Locate every malaria parasite.
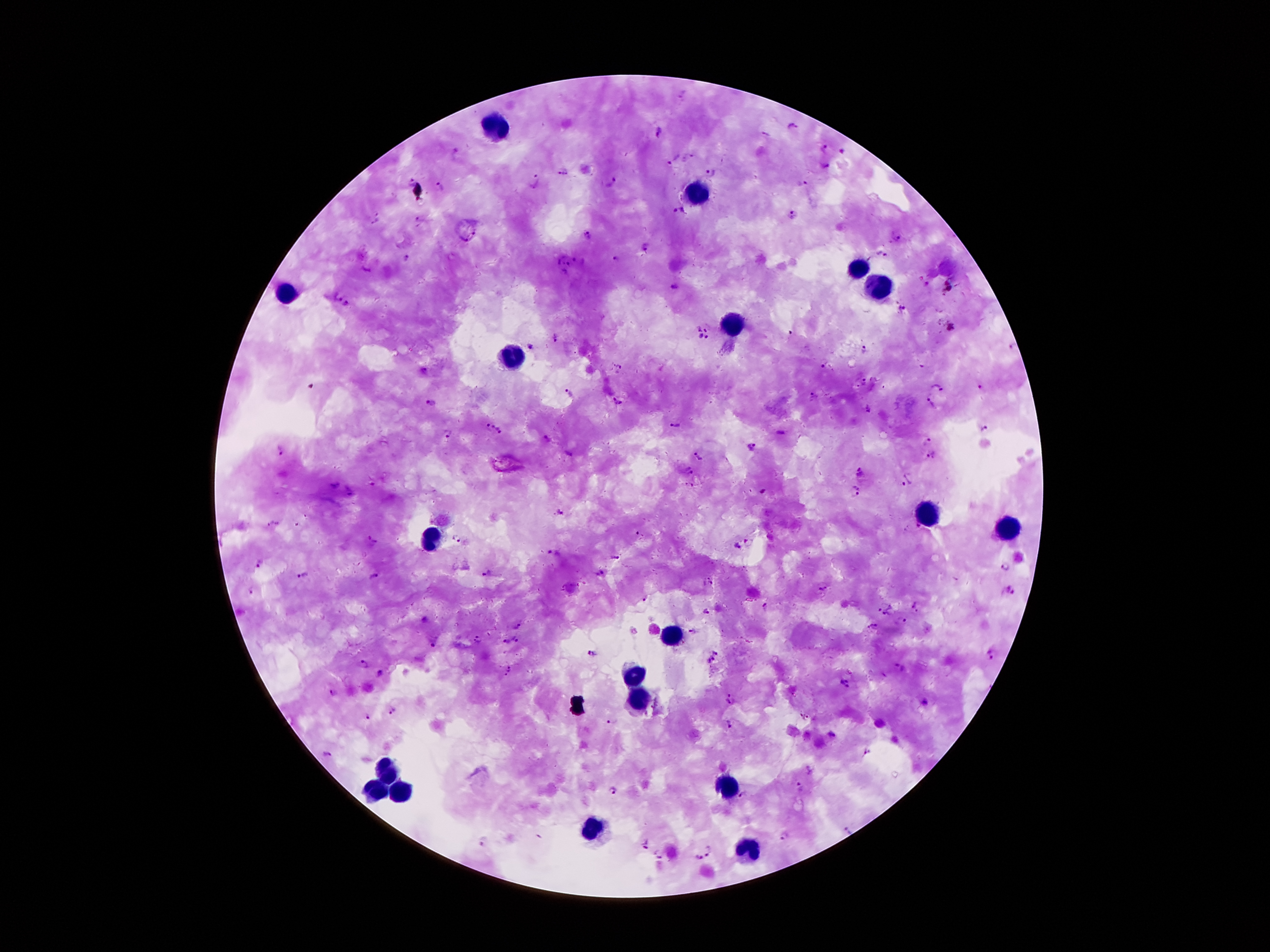

Approximate centers as {x, y} in pixels.
Malaria parasites: {683, 95}, {792, 126}, {660, 132}, {765, 135}, {825, 147}, {842, 151}, {674, 160}, {825, 168}, {563, 173}, {711, 173}, {538, 176}, {613, 181}, {412, 182}, {801, 183}, {441, 188}, {677, 211}, {794, 214}, {375, 217}, {420, 219}, {588, 236}, {897, 239}, {646, 247}, {881, 254}, {618, 258}, {407, 259}, {578, 259}, {567, 264}, {675, 287}, {345, 303}, {900, 309}, {701, 334}, {554, 337}, {529, 347}, {1010, 347}, {863, 349}, {824, 364}, {620, 368}, {424, 373}, {865, 382}, {936, 386}, {980, 388}, {568, 395}, {814, 396}, {930, 396}, {430, 402}, {618, 403}, {867, 409}, {488, 426}, {674, 426}, {984, 429}, {449, 433}, {503, 433}, {780, 433}, {547, 438}, {927, 441}, {753, 447}, {281, 450}, {569, 454}, {697, 456}, {932, 456}, {689, 471}, {859, 474}, {907, 479}, {690, 486}, {763, 491}, {856, 492}, {558, 512}, {274, 524}, {918, 528}, {458, 537}, {372, 541}, {737, 546}, {554, 554}, {616, 558}, {259, 565}, {1004, 568}, {487, 573}, {600, 574}, {303, 576}, {375, 578}, {708, 582}, {824, 588}, {1009, 590}, {250, 591}, {645, 597}, {916, 606}, {764, 607}, {886, 607}, {707, 611}, {902, 622}, {516, 625}, {872, 626}, {692, 631}, {480, 639}, {516, 640}, {507, 641}, {433, 645}, {713, 652}, {592, 654}, {989, 654}, {711, 660}, {364, 664}, {900, 668}, {509, 670}, {381, 674}, {844, 685}, {333, 693}, {732, 700}, {925, 703}, {393, 711}, {365, 716}, {806, 717}, {612, 721}, {729, 726}, {831, 735}, {327, 753}, {800, 788}, {614, 792}, {745, 796}, {848, 831}, {785, 836}, {482, 841}, {645, 847}, {711, 851}, {658, 855}, {696, 858}.

patient_malaria_status: positive for Plasmodium falciparum
stain: Giemsa
capture: smartphone camera through the microscope eyepiece
field_of_view: single
image_size: 1270×952 pixels
magnification: 100x
leukocyte_locations: 'approximate centers as {x, y} in pixels: {497, 128}, {699, 194}, {855, 269}, {876, 289}, {287, 294}, {731, 326}, {510, 357}, {928, 512}, {1008, 530}, {429, 539}, {669, 637}, {631, 676}, {637, 700}, {385, 767}, {728, 787}, {401, 789}, {376, 792}, {594, 828}, {749, 851}'
preparation: thick blood smear